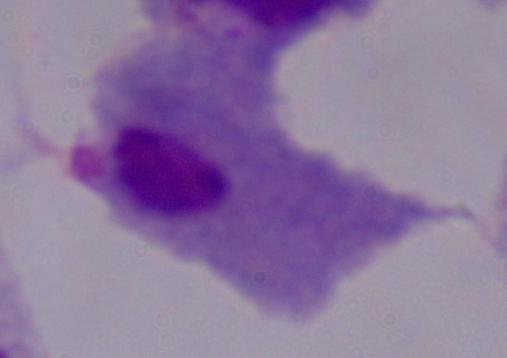
modality = photomicrograph
identification = trichomonad
magnification = 1000x